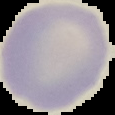

Segmented cell region on a black background. From a thin blood film. Malaria status: uninfected. Image is 115×115 pixels.